Give the position of every Plasmodium parasite.
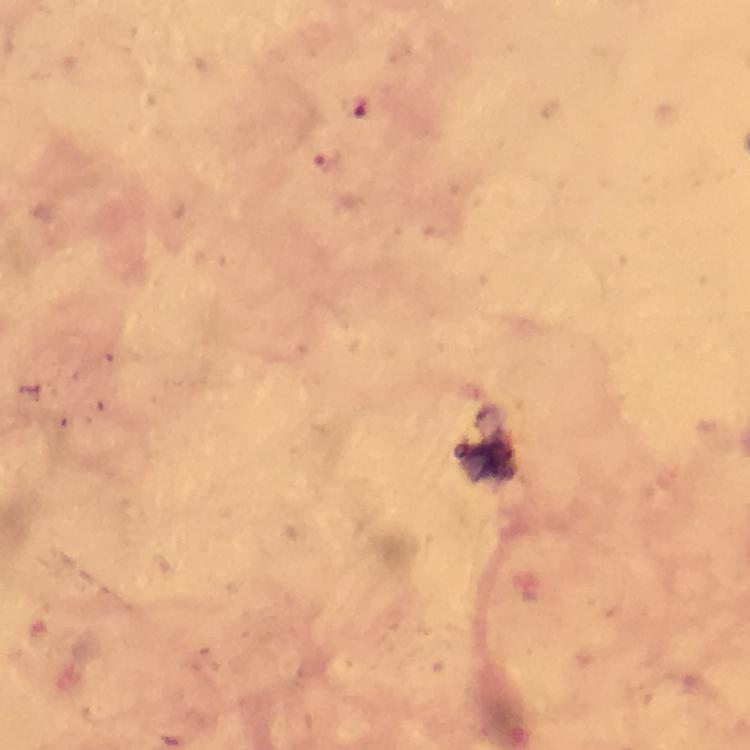

Approximate object centers, in pixels from the top-left corner.
Plasmodium parasites: (x=351, y=105), (x=329, y=161).

Summary:
  - Cropped from: a single field of view
  - Image size: 750×750 pixels
  - Preparation: thick blood smear
  - Capture: smartphone mounted on the microscope
  - Immersion oil: used
  - Context: from a diagnostic examination for malaria
  - Magnification: 100x
  - Stain: Giemsa